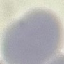

{
  "malaria_status": "uninfected",
  "capture": "smartphone through the microscope eyepiece",
  "stain": "Giemsa",
  "image_type": "automatically extracted cell patch, resized to 64 × 64 pixels",
  "preparation": "thin smear"
}